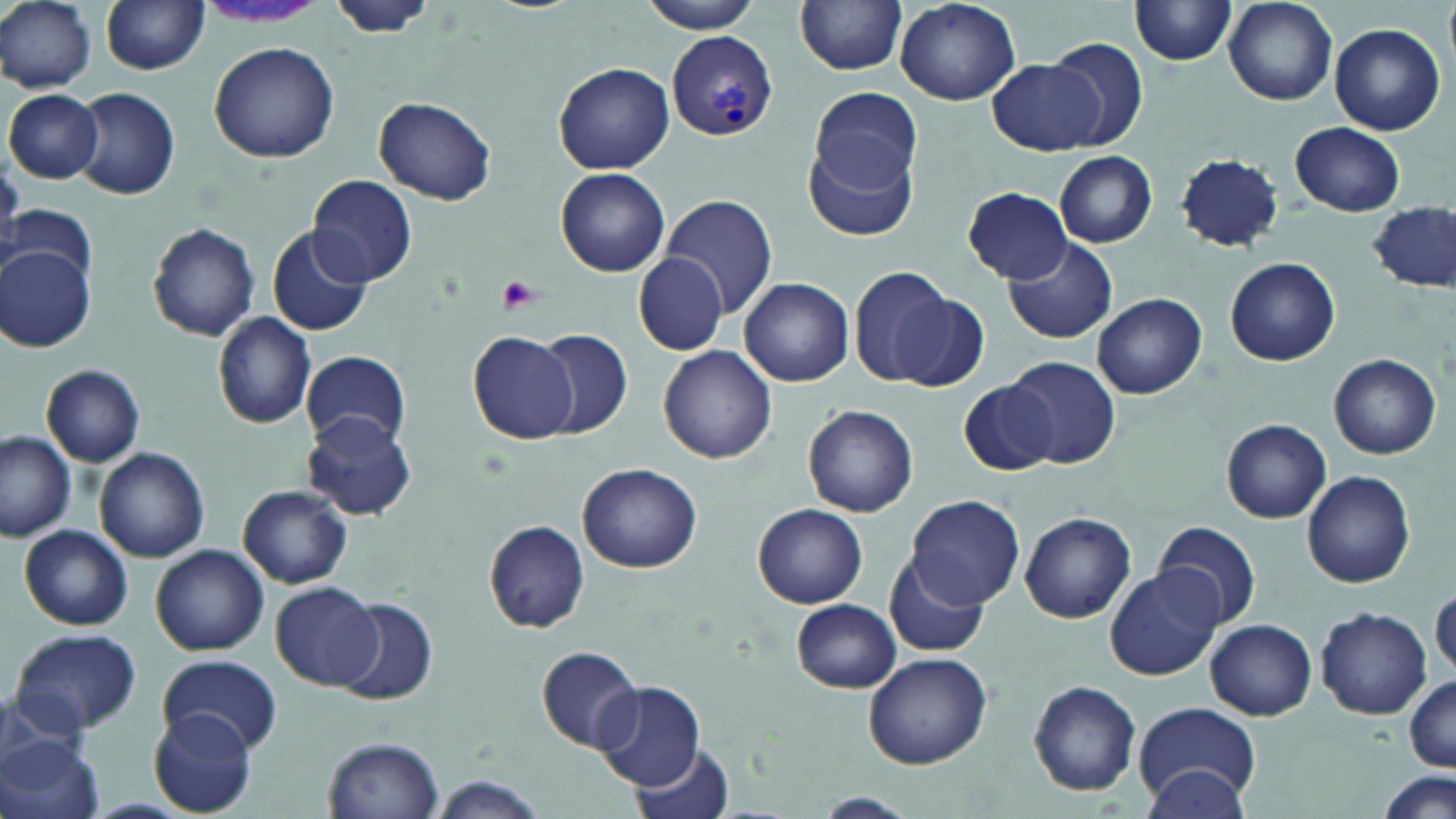

{
  "slide_level_diagnosis": "Plasmodium vivax",
  "preparation": "thin blood smear",
  "field_of_view": "single",
  "magnification": "1000x",
  "modality": "optical microscopy",
  "stain": "May-Grünwald-Giemsa",
  "image_size": "1456×819 pixels",
  "plasmodium_vivax_infected_red_blood_cell_locations": "approximate bounding boxes as [x1, y1, x2, y2] in pixels: [668, 31, 776, 141]",
  "uninfected_red_blood_cell_locations": "approximate bounding boxes as [x1, y1, x2, y2] in pixels: [0, 0, 97, 92], [327, 0, 439, 39], [640, 0, 764, 34], [795, 0, 908, 74], [101, 1, 210, 74], [895, 1, 1022, 106], [1130, 1, 1235, 66], [1223, 2, 1336, 104], [1328, 23, 1446, 136], [1046, 36, 1150, 150], [209, 42, 339, 164], [988, 58, 1103, 155], [554, 62, 675, 173], [71, 87, 179, 199], [810, 87, 922, 192], [5, 89, 103, 183], [373, 98, 497, 205], [1290, 122, 1405, 216], [805, 137, 919, 243], [1054, 150, 1157, 247], [1174, 153, 1283, 252], [555, 167, 670, 276], [306, 176, 417, 288], [961, 187, 1073, 282], [659, 194, 778, 320], [4, 204, 97, 288], [1368, 204, 1455, 292], [149, 222, 260, 341], [267, 225, 373, 338], [1004, 237, 1118, 344], [1, 248, 94, 352], [632, 254, 731, 355], [1225, 257, 1339, 365], [847, 266, 955, 388], [738, 277, 853, 387], [890, 288, 988, 392], [1091, 293, 1208, 399], [212, 312, 318, 430], [534, 328, 632, 439], [467, 330, 580, 444], [658, 345, 777, 465], [301, 350, 410, 452], [1328, 353, 1442, 459], [1007, 354, 1121, 469], [41, 364, 145, 467], [959, 378, 1059, 476], [803, 404, 919, 517], [303, 414, 415, 519], [1222, 419, 1331, 524], [1, 432, 77, 541], [94, 447, 208, 563], [578, 464, 702, 574], [1301, 471, 1415, 587], [239, 485, 352, 588], [906, 495, 1024, 609], [751, 503, 868, 609], [1019, 512, 1137, 622], [1154, 519, 1260, 632], [484, 520, 590, 633], [20, 526, 133, 631], [151, 544, 269, 656], [883, 554, 988, 659], [1106, 566, 1224, 681], [272, 581, 385, 690], [1431, 590, 1455, 677], [333, 600, 438, 705], [791, 600, 902, 693], [1316, 607, 1431, 719], [1206, 619, 1316, 719], [10, 628, 142, 735], [537, 645, 645, 753], [862, 650, 990, 768], [157, 655, 284, 756], [1404, 674, 1456, 772], [1029, 681, 1140, 796], [0, 682, 98, 774], [595, 683, 703, 791], [1133, 702, 1263, 807], [147, 710, 259, 816], [0, 735, 104, 819], [323, 736, 443, 818], [630, 741, 736, 819], [1142, 764, 1252, 818], [1377, 771, 1454, 819], [425, 777, 549, 818], [817, 792, 915, 816]",
  "platelet_locations": "approximate bounding boxes as [x1, y1, x2, y2] in pixels: [500, 275, 541, 313]"
}